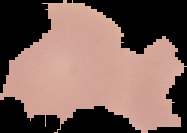
Summary:
  - Image size: 187×133 pixels
  - Image type: cell region segmented out of the field of view; surrounding area masked to black
  - Result: no malaria parasites detected
  - Preparation: thin blood smear